State the blood parasite species.
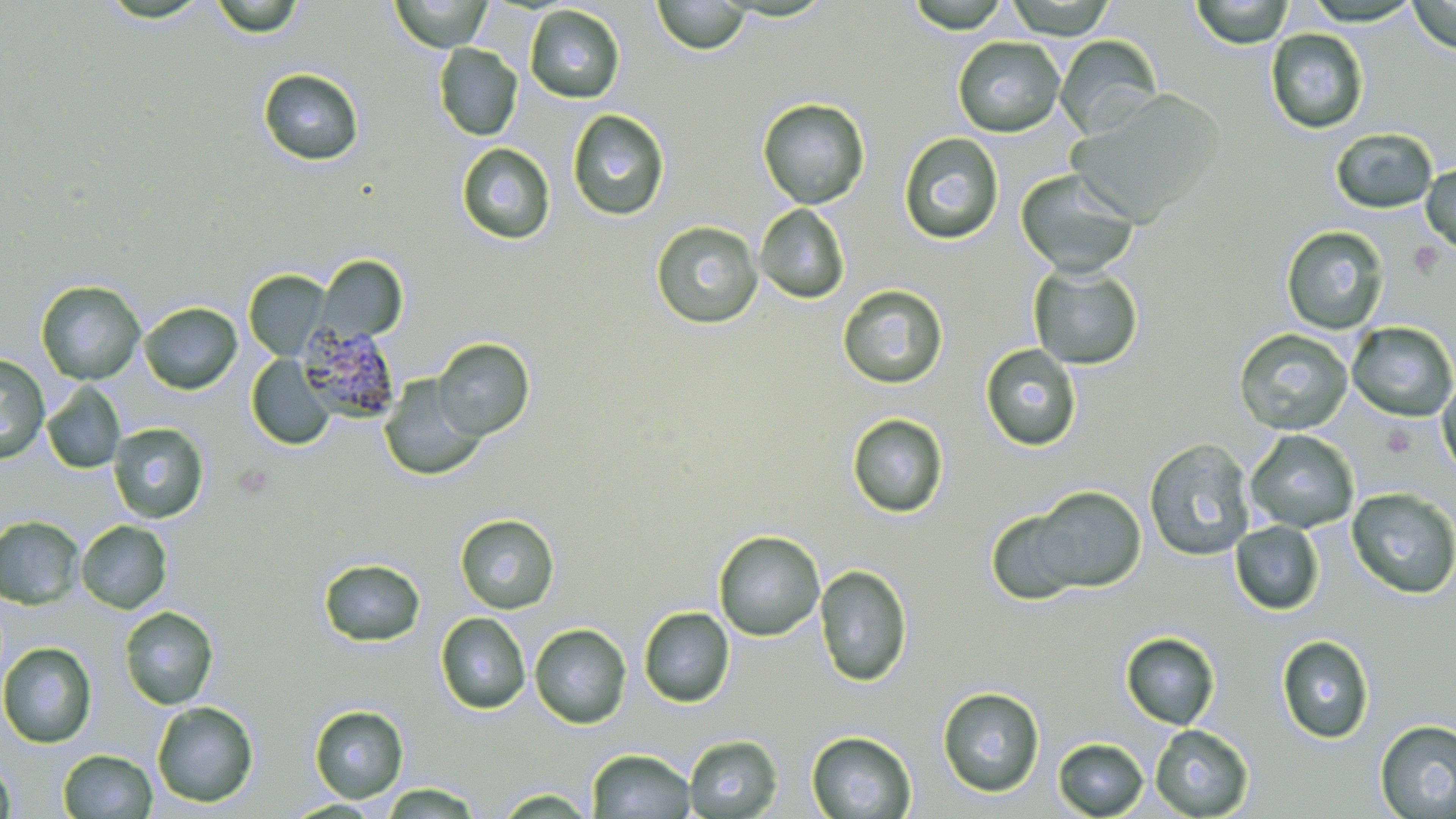

Plasmodium malariae.

Summary:
  - Coordinate format: approximate bounding boxes as (x1, y1, x2, y2) in pixels
  - Platelet locations: (1410, 242, 1444, 277)
  - Uninfected red blood cell locations: (96, 0, 213, 25), (210, 0, 305, 38), (390, 0, 492, 51), (652, 0, 750, 55), (905, 0, 1011, 33), (1004, 0, 1117, 39), (1190, 0, 1293, 48), (1301, 0, 1423, 26), (1407, 0, 1456, 54), (525, 5, 625, 103), (1265, 29, 1369, 134), (1054, 35, 1162, 139), (953, 36, 1065, 137), (433, 43, 523, 141), (258, 68, 364, 166), (1068, 90, 1224, 225), (757, 98, 870, 209), (567, 109, 670, 221), (1331, 128, 1438, 214), (898, 132, 1004, 244), (457, 143, 556, 245), (1421, 164, 1456, 254), (1015, 169, 1140, 278), (755, 204, 850, 304), (650, 221, 763, 329), (1281, 226, 1390, 334), (317, 256, 407, 342), (1028, 265, 1144, 370), (244, 270, 330, 360), (35, 281, 146, 385), (836, 284, 949, 389), (139, 302, 242, 395), (1346, 321, 1456, 422), (1233, 328, 1353, 435), (432, 338, 535, 440), (979, 343, 1082, 452), (0, 355, 50, 463), (246, 355, 336, 450), (1437, 372, 1456, 481), (379, 376, 487, 481), (41, 382, 126, 474), (846, 413, 949, 518), (108, 423, 209, 522), (1245, 429, 1359, 533), (1144, 438, 1255, 561), (1026, 486, 1146, 593), (1347, 487, 1456, 599), (986, 508, 1088, 606), (454, 513, 560, 615), (0, 516, 84, 609), (76, 520, 172, 614), (1230, 521, 1324, 615), (713, 530, 825, 641), (318, 558, 426, 647), (814, 564, 913, 687), (119, 606, 219, 709), (638, 607, 735, 707), (435, 612, 530, 714), (529, 623, 632, 729), (1120, 632, 1220, 730), (1276, 635, 1375, 743), (0, 642, 97, 748), (937, 686, 1045, 798), (152, 701, 259, 807), (310, 705, 409, 802), (1374, 719, 1456, 818), (1150, 724, 1254, 818), (806, 731, 917, 818), (683, 735, 783, 819), (1053, 737, 1149, 818), (588, 748, 696, 818), (58, 750, 158, 818), (0, 755, 15, 819), (376, 782, 487, 818), (492, 788, 597, 817), (283, 798, 387, 817)
  - Plasmodium malariae-infected red blood cell locations: (298, 326, 402, 422)
  - Field of view: single
  - Stain: May-Grünwald-Giemsa
  - Magnification: 1000x
  - Modality: light microscopy
  - Preparation: thin blood smear
  - Image size: 1456×819 pixels